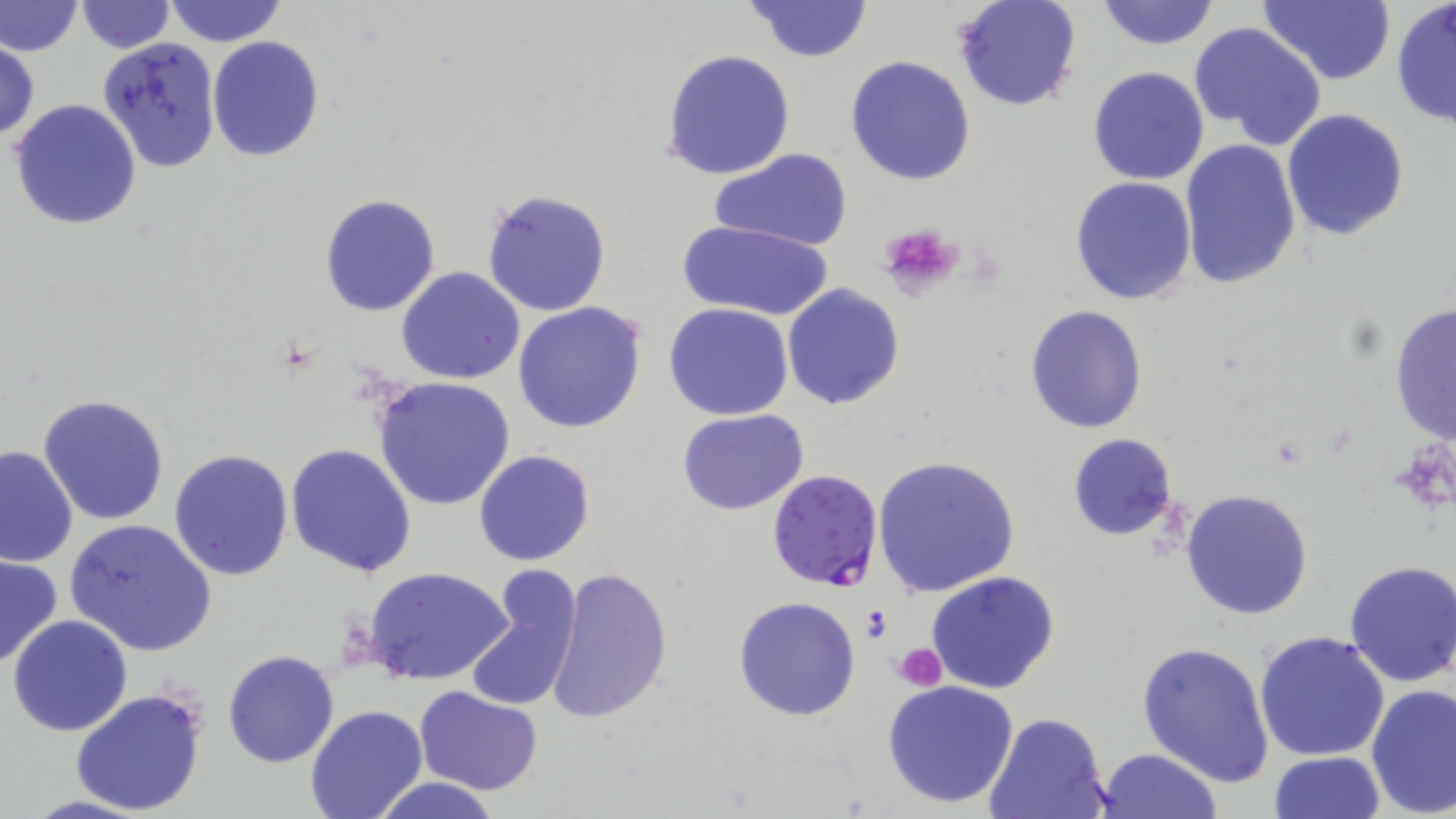
slide_level_diagnosis: Plasmodium falciparum
platelet_locations: 'approximate bounding boxes as (x1, y1, x2, y2) in pixels: (878, 222, 965, 297), (862, 603, 892, 642), (894, 643, 947, 690)'
plasmodium_falciparum_infected_red_blood_cell_locations: 'approximate bounding boxes as (x1, y1, x2, y2) in pixels: (767, 469, 885, 593)'
preparation: thin blood film
image_size: 1456×819 pixels
uninfected_red_blood_cell_locations: 'approximate bounding boxes as (x1, y1, x2, y2) in pixels: (1, 0, 82, 58), (163, 0, 287, 48), (952, 0, 1083, 112), (1097, 0, 1219, 50), (74, 1, 175, 53), (744, 1, 873, 62), (1258, 1, 1395, 86), (1390, 3, 1456, 128), (1190, 20, 1327, 150), (98, 36, 223, 173), (207, 36, 324, 160), (1, 40, 40, 141), (661, 48, 796, 180), (845, 54, 975, 185), (1088, 66, 1211, 185), (9, 99, 142, 231), (1281, 108, 1410, 242), (1179, 141, 1303, 292), (711, 149, 853, 251), (1070, 176, 1198, 306), (482, 188, 611, 318), (320, 194, 440, 317), (678, 219, 833, 321), (396, 265, 525, 384), (781, 283, 905, 410), (1387, 300, 1456, 449), (513, 302, 647, 434), (663, 303, 794, 421), (1025, 304, 1147, 433), (374, 375, 518, 510), (38, 394, 169, 525), (677, 409, 809, 515), (1068, 434, 1179, 541), (287, 442, 417, 577), (0, 443, 78, 567), (473, 448, 596, 566), (169, 449, 293, 580), (873, 454, 1023, 598), (1181, 488, 1314, 619), (63, 518, 217, 656), (1, 553, 64, 669), (1343, 562, 1456, 687), (545, 565, 674, 724), (363, 566, 514, 687), (464, 567, 585, 713), (925, 570, 1061, 696), (732, 596, 861, 721), (6, 616, 132, 736), (1256, 630, 1390, 761), (1137, 640, 1276, 786), (222, 649, 339, 768), (882, 679, 1022, 809), (1365, 684, 1455, 816), (415, 686, 545, 797), (70, 687, 207, 817), (304, 704, 429, 819), (982, 712, 1112, 819), (1093, 748, 1223, 819), (1267, 751, 1384, 819), (368, 777, 505, 819)'
modality: light microscopy
magnification: 1000x
stain: May-Grünwald-Giemsa
field_of_view: one of a larger specimen